State which cell type is depicted.
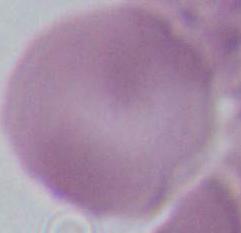

This is an erythrocyte.

Summary:
  - Magnification: 1000x
  - Modality: photomicrograph